Give the preparation type.
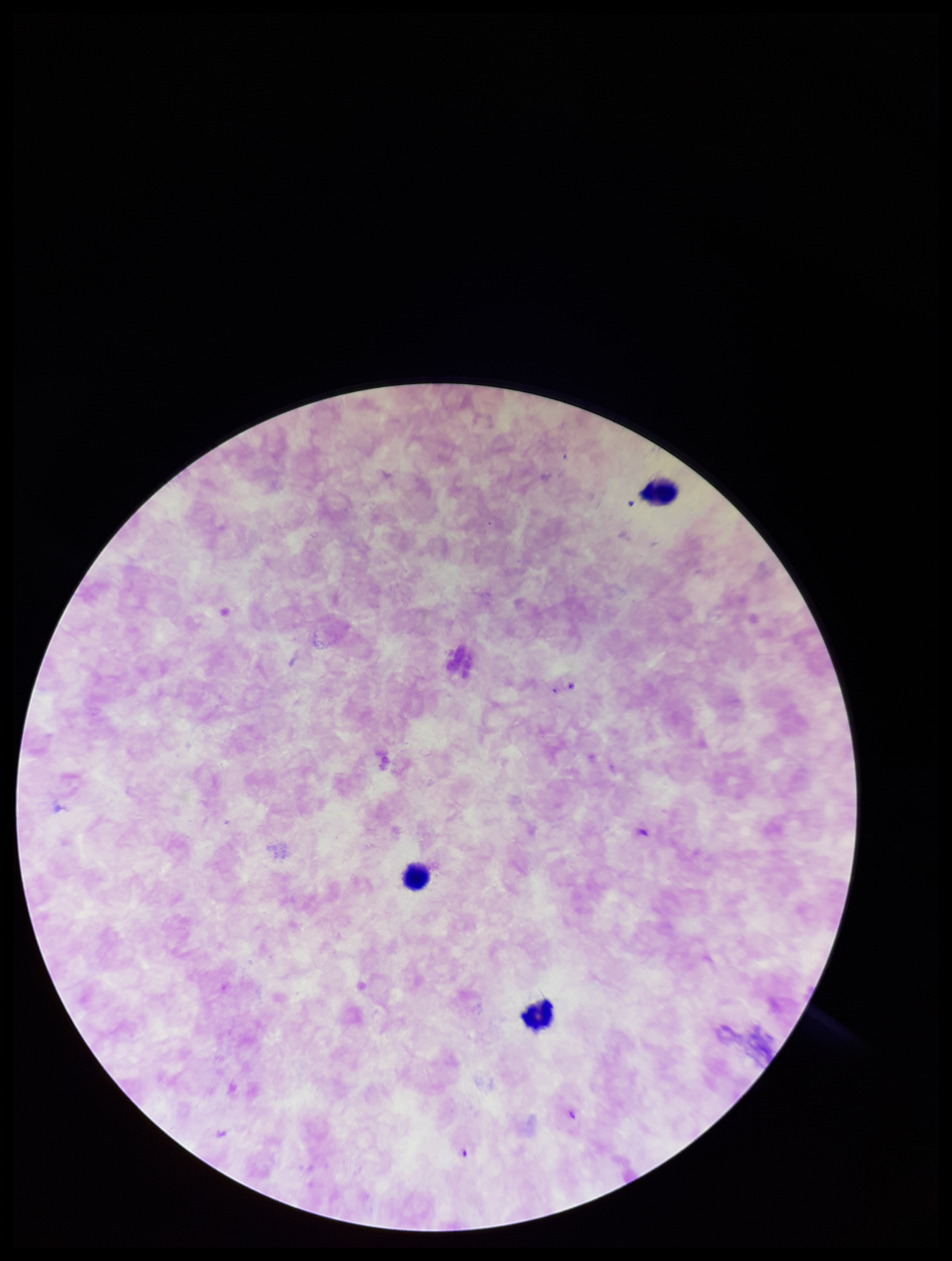
It is a thick blood smear.

Summary:
  - Species reported for this patient: Plasmodium falciparum
  - Field of view: one from this slide
  - Image size: 952×1261 pixels
  - Capture: smartphone photograph through the microscope eyepiece
  - Plasmodium parasites: identified
  - Stain: Giemsa
  - Patient malaria status: infected
  - Leukocyte count: 3
  - Parasite count: 2